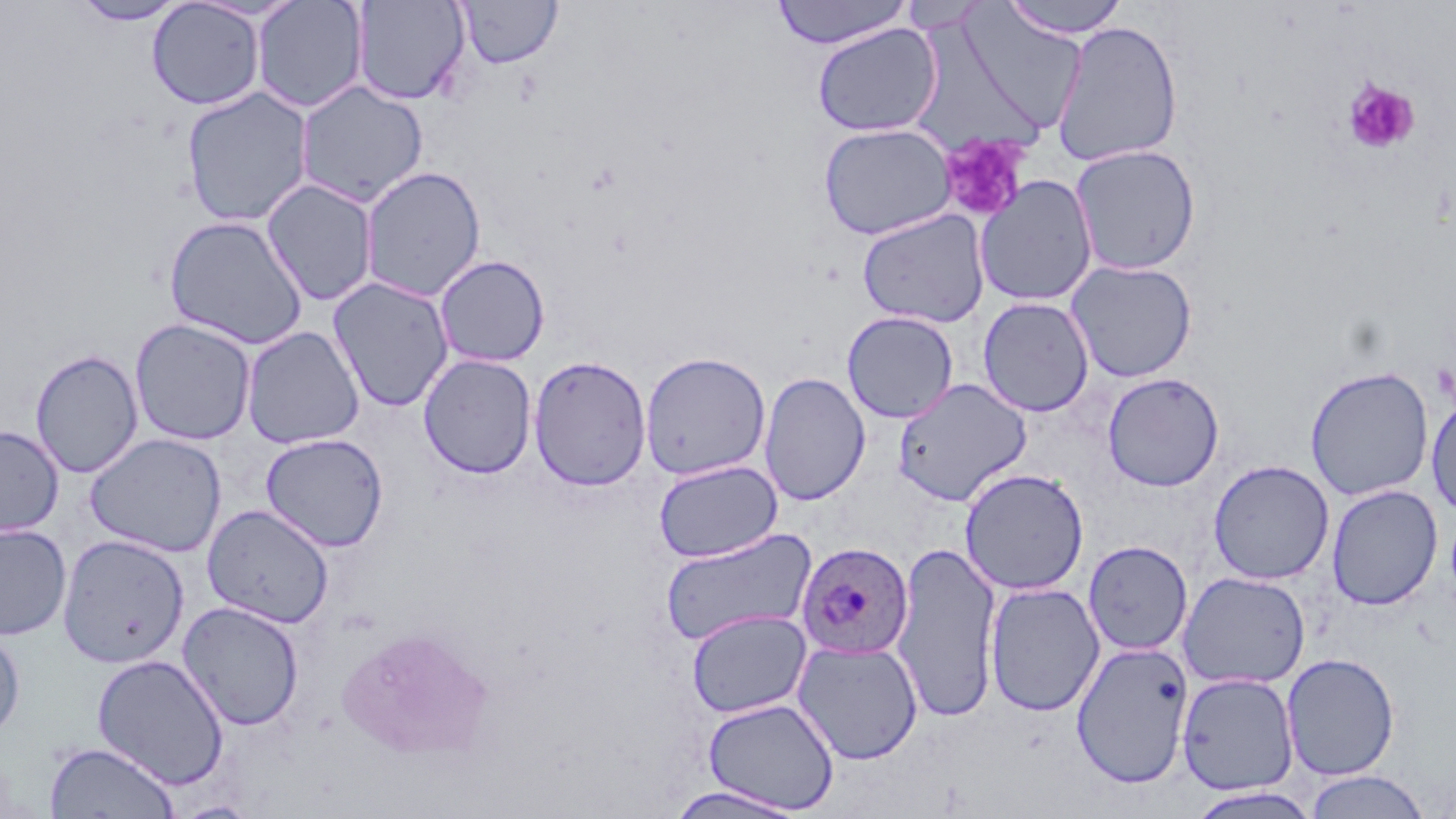
slide-level diagnosis = Plasmodium ovale
platelet locations = approximate bounding boxes as (x1, y1, x2, y2) in pixels: (1342, 77, 1420, 154), (938, 134, 1030, 223)
field of view = one of a larger specimen
modality = light microscopy
uninfected red blood cell locations = approximate bounding boxes as (x1, y1, x2, y2) in pixels: (71, 0, 188, 26), (252, 0, 369, 114), (770, 0, 913, 50), (1000, 0, 1131, 39), (147, 1, 265, 110), (352, 1, 470, 105), (458, 1, 562, 69), (898, 1, 988, 34), (952, 5, 1086, 138), (1051, 20, 1184, 167), (812, 22, 942, 138), (295, 80, 429, 207), (181, 87, 315, 228), (818, 123, 956, 240), (1069, 144, 1202, 275), (359, 165, 487, 302), (974, 175, 1098, 307), (261, 179, 378, 307), (856, 208, 990, 328), (163, 215, 308, 350), (434, 254, 550, 367), (1065, 259, 1198, 382), (327, 276, 454, 412), (977, 297, 1094, 417), (842, 311, 959, 424), (129, 318, 257, 446), (241, 326, 365, 449), (31, 349, 144, 478), (639, 351, 771, 481), (419, 353, 537, 479), (528, 355, 652, 492), (1305, 366, 1434, 501), (759, 372, 870, 506), (1102, 372, 1224, 491), (893, 377, 1032, 506), (1427, 393, 1456, 520), (0, 426, 64, 536), (84, 432, 227, 558), (260, 433, 389, 552), (1208, 459, 1334, 585), (653, 460, 782, 563), (959, 468, 1089, 595), (1326, 484, 1443, 610), (202, 504, 334, 628), (0, 523, 72, 640), (658, 527, 817, 647), (57, 535, 189, 668), (1083, 540, 1193, 655), (891, 541, 1003, 723), (1178, 571, 1311, 690), (984, 582, 1105, 716), (177, 600, 305, 731), (686, 608, 811, 718), (0, 627, 25, 741), (793, 640, 923, 764), (1071, 641, 1194, 788), (1282, 653, 1400, 781), (92, 654, 230, 790), (1176, 672, 1300, 796), (703, 697, 839, 814), (44, 741, 179, 818), (1303, 770, 1432, 818), (665, 785, 808, 819), (1186, 787, 1323, 819), (170, 800, 262, 818)
stain = May-Grünwald-Giemsa
magnification = 1000x
preparation = thin blood film
image size = 1456×819 pixels
Plasmodium ovale-infected red blood cell locations = approximate bounding boxes as (x1, y1, x2, y2) in pixels: (796, 541, 914, 660)